Classify this cell by malaria status.
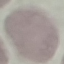
It is uninfected.

Photographed with a smartphone camera at the microscope eyepiece. Giemsa stain. Thin blood smear. Automatically extracted cell patch, resized to 64 × 64 pixels.